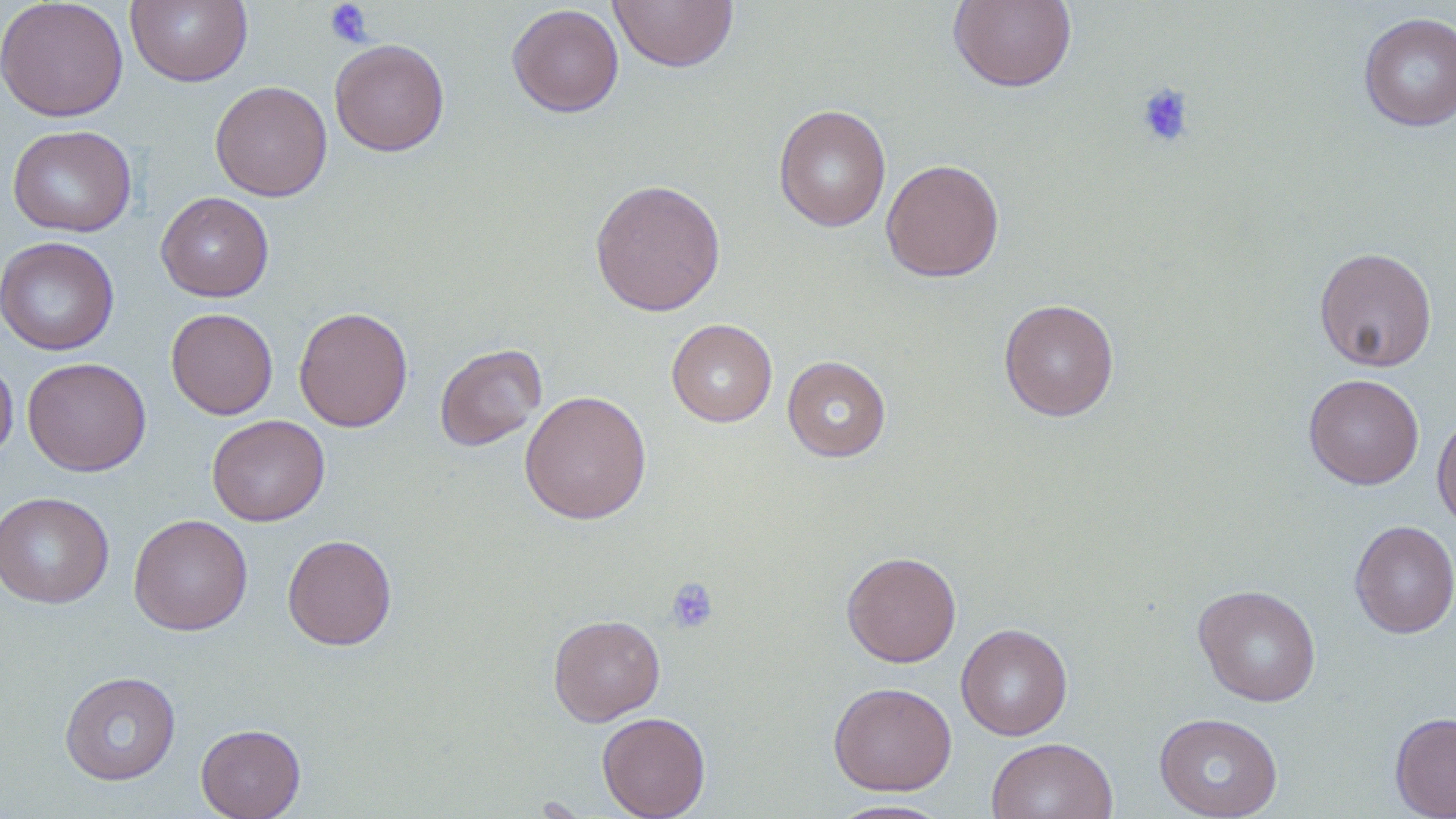

Summary:
  - Coordinate format: approximate bounding boxes as [x1, y1, x2, y2] in pixels
  - Platelet locations: [324, 0, 373, 48], [1135, 82, 1196, 148], [664, 577, 719, 634]
  - Uninfected red blood cell locations: [0, 0, 128, 122], [125, 0, 253, 87], [948, 0, 1077, 92], [609, 1, 738, 72], [507, 3, 624, 117], [1358, 12, 1455, 132], [330, 38, 450, 157], [209, 80, 332, 201], [774, 104, 891, 232], [7, 124, 137, 237], [880, 159, 1005, 282], [589, 178, 726, 317], [156, 192, 274, 302], [1, 235, 119, 355], [1314, 247, 1438, 372], [998, 298, 1120, 422], [294, 306, 413, 432], [166, 308, 278, 420], [666, 319, 777, 427], [434, 343, 547, 451], [0, 354, 18, 463], [782, 355, 891, 462], [22, 357, 151, 476], [1303, 373, 1424, 490], [519, 389, 652, 525], [1432, 410, 1456, 531], [207, 414, 330, 526], [0, 491, 114, 609], [128, 514, 252, 635], [1349, 519, 1456, 639], [282, 534, 397, 650], [841, 551, 962, 667], [1193, 584, 1322, 706], [548, 614, 665, 726], [956, 623, 1073, 741], [59, 671, 181, 785], [828, 681, 957, 795], [597, 712, 711, 819], [1390, 712, 1456, 818], [1154, 713, 1283, 819], [195, 723, 306, 819], [986, 737, 1118, 819], [827, 798, 954, 818]
  - Slide-level diagnosis: negative for blood parasites
  - Preparation: thin blood smear
  - Stain: May-Grünwald-Giemsa
  - Modality: light microscopy
  - Image size: 1456×819 pixels
  - Field of view: one of a larger specimen
  - Magnification: 1000x